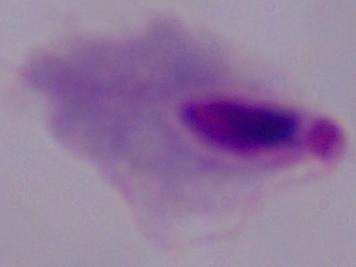

A trichomonad is shown. Captured at 1000x magnification. Photomicrograph.